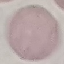

Malaria status: uninfected. Thin blood smear. Automatically extracted cell patch, resized to 64 × 64 pixels. Giemsa-stained preparation. Acquired by smartphone through the microscope eyepiece.